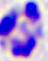

modality = photomicrograph
magnification = 400x
identification = leukocyte